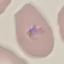
Summary:
  - Result: malaria parasites detected
  - Preparation: thin smear
  - Capture: smartphone camera at the microscope eyepiece
  - Image type: automatically extracted cell patch, resized to 64 × 64 pixels
  - Stain: Giemsa